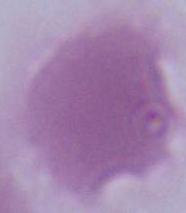

Summary:
  - Magnification: 1000x
  - Modality: photomicrograph
  - Identification: erythrocyte